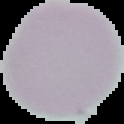

preparation: thin blood film
image_size: 124×124 pixels
malaria_status: uninfected
image_type: segmented cell region with the area outside set to black